Describe the morphology of the erythrocytes.
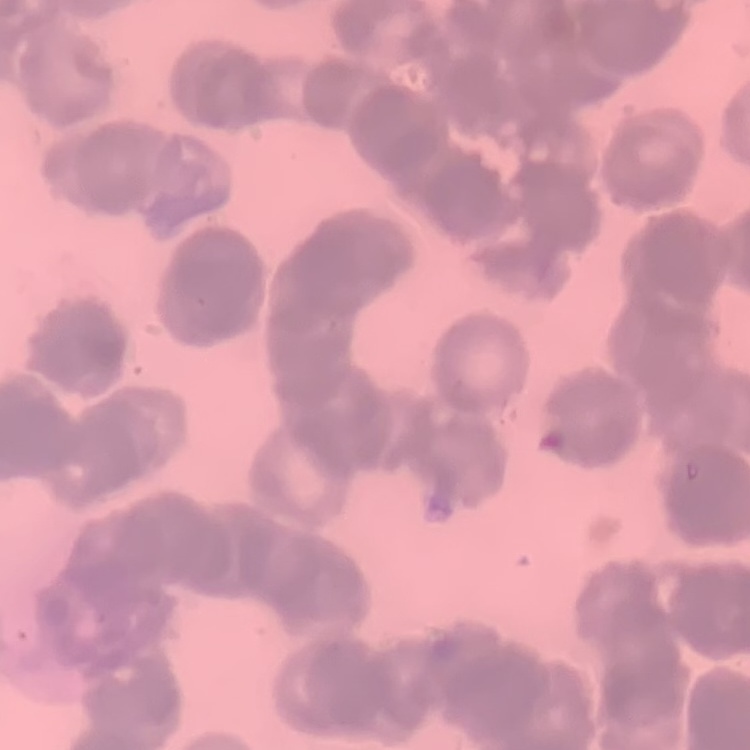
They show rouleaux formation.

Summary:
  - Preparation: thin blood smear
  - Stain: Field's or Giemsa
  - Image type: one tile cut from a larger photomicrograph